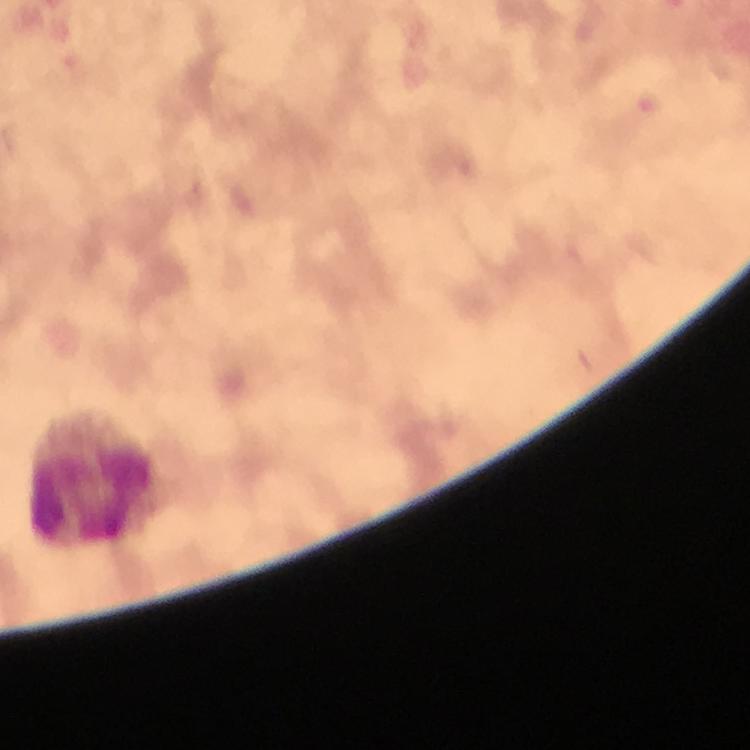
Approximate object centers, in pixels from the top-left corner.
Summary:
  - Leukocyte locations: (x=92, y=481)
  - Plasmodium parasites: none seen
  - Image size: 750×750 pixels
  - Preparation: thick blood film
  - Cropped from: a single field of view
  - Capture: smartphone camera through the microscope
  - Magnification: 100x
  - Stain: Giemsa
  - Context: from a diagnostic examination for malaria
  - Immersion oil: used